Name the parasite shown.
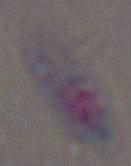
Toxoplasma gondii.

magnification: 1000x
modality: photomicrograph